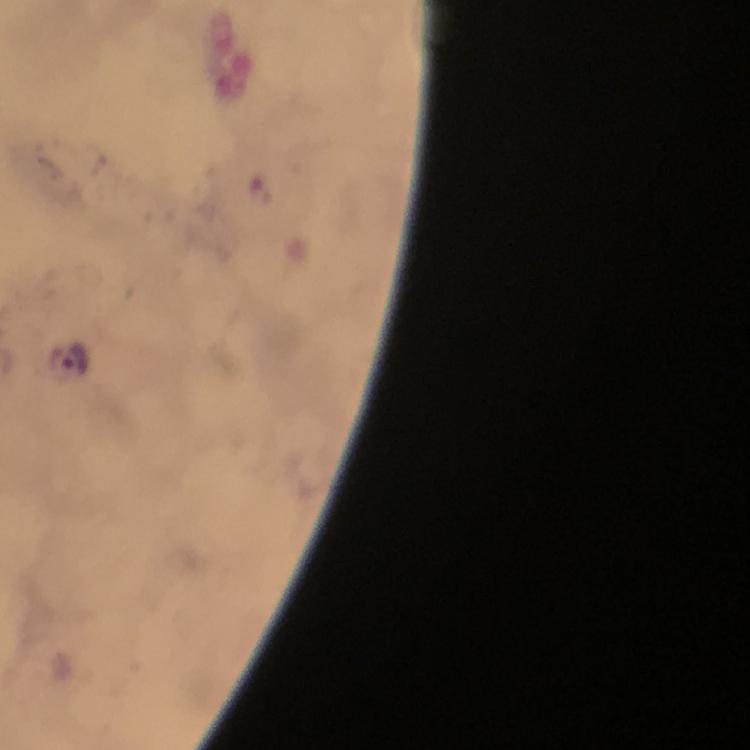

context: from a diagnostic examination for malaria
capture: smartphone camera through the microscope
preparation: thick blood smear
plasmodium_parasite_locations: 'approximate centers as {x, y} in pixels: {69, 358}'
magnification: 100x
cropped_from: one field of view
immersion_oil: used
stain: Giemsa
image_size: 750×750 pixels